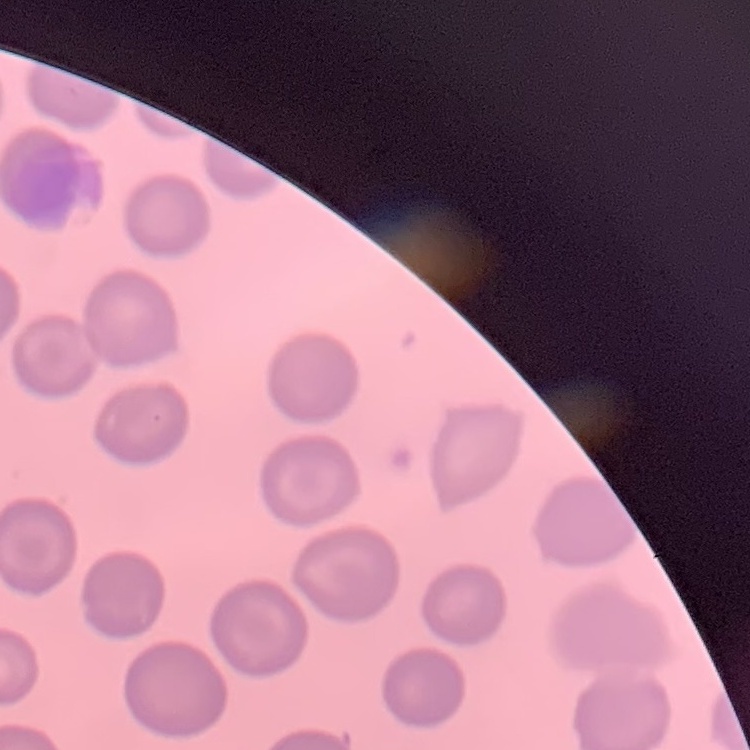
Summary:
  - Erythrocyte morphology: no rouleaux formation
  - Stain: Field's or Giemsa
  - Image type: square crop of a larger photomicrograph
  - Preparation: thin blood film